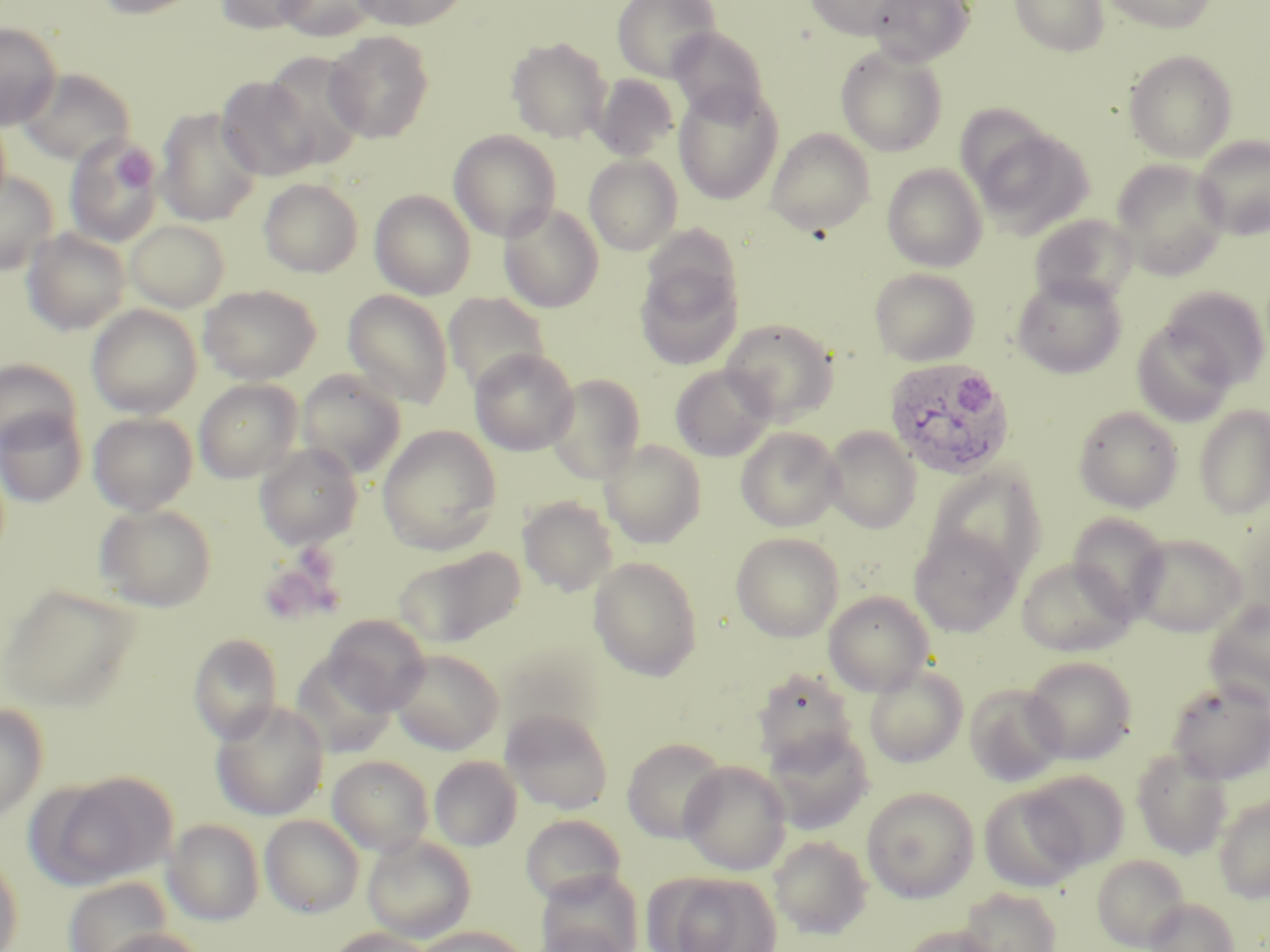
Approximate bounding boxes as (x1, y1, x2, y2) in pixels. Uninfected red blood cell locations: (93, 0, 203, 18), (213, 0, 316, 34), (273, 0, 382, 41), (351, 0, 471, 30), (612, 0, 722, 81), (803, 0, 916, 40), (867, 0, 975, 67), (1009, 0, 1110, 57), (1100, 0, 1216, 33), (0, 22, 62, 130), (669, 27, 769, 123), (324, 30, 434, 144), (507, 37, 612, 144), (835, 46, 948, 157), (259, 50, 368, 167), (1124, 50, 1237, 163), (18, 68, 136, 166), (592, 74, 679, 162), (216, 75, 322, 182), (673, 86, 783, 205), (954, 103, 1055, 196), (155, 107, 262, 227), (765, 128, 876, 236), (448, 130, 561, 242), (975, 130, 1092, 237), (1192, 134, 1270, 240), (64, 137, 164, 246), (584, 154, 682, 255), (1111, 159, 1229, 279), (882, 163, 987, 272), (0, 172, 59, 275), (258, 178, 363, 278), (370, 190, 475, 300), (499, 203, 604, 313), (1028, 214, 1138, 307), (126, 219, 230, 311), (23, 228, 131, 334), (636, 264, 742, 369), (870, 267, 979, 366), (1010, 273, 1127, 379), (198, 284, 321, 384), (1159, 284, 1270, 387), (342, 289, 454, 410), (443, 292, 550, 395), (87, 304, 202, 418), (720, 318, 839, 424), (1131, 319, 1236, 427), (469, 348, 578, 456), (0, 359, 82, 453), (671, 365, 775, 461), (297, 368, 406, 477), (546, 373, 645, 483), (194, 379, 302, 483), (1193, 405, 1270, 520), (1073, 406, 1183, 512), (0, 408, 87, 507), (88, 412, 198, 515), (377, 425, 502, 555), (823, 426, 921, 532), (736, 427, 843, 532), (600, 439, 706, 549), (254, 443, 364, 550), (927, 466, 1046, 582), (518, 497, 619, 596), (95, 504, 217, 612), (1067, 512, 1170, 622), (909, 527, 1022, 637), (731, 533, 844, 642), (1130, 534, 1247, 636), (397, 547, 522, 646), (588, 557, 703, 681), (1017, 557, 1136, 657), (1, 584, 140, 710), (823, 591, 934, 695), (1204, 598, 1270, 708), (322, 614, 430, 715), (188, 633, 283, 744), (389, 649, 504, 755), (290, 653, 397, 757), (1022, 656, 1137, 764), (864, 665, 968, 768), (752, 668, 858, 770), (1165, 679, 1270, 784), (965, 683, 1067, 787), (210, 701, 329, 821), (0, 703, 48, 824), (501, 708, 614, 815), (762, 726, 874, 834), (622, 737, 727, 843), (1132, 749, 1233, 860), (328, 755, 434, 857), (429, 756, 523, 851), (679, 761, 791, 875), (1023, 771, 1130, 870), (40, 772, 178, 888), (979, 786, 1089, 892), (861, 787, 979, 902), (1214, 795, 1270, 903), (520, 814, 627, 907), (260, 815, 364, 917), (163, 819, 265, 925), (362, 835, 476, 942), (769, 835, 872, 939), (0, 853, 23, 952), (1092, 854, 1190, 951), (654, 872, 781, 952), (63, 877, 171, 952), (535, 883, 641, 952), (958, 886, 1062, 952), (1144, 898, 1238, 952), (532, 922, 637, 952), (896, 925, 1003, 952), (413, 926, 530, 952), (95, 927, 209, 952), (324, 927, 435, 952). Plasmodium ovale-infected red blood cell locations: (885, 357, 1016, 479). Platelet locations: (114, 150, 154, 191), (258, 551, 345, 626). Slide-level diagnosis: Plasmodium ovale. Light microscopy. Image is 1270×952 pixels. May-Grünwald-Giemsa-stained preparation. Captured at 1000x magnification. One field of a larger specimen. Thin blood film.